Classify this cell by malaria status.
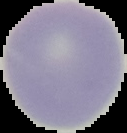

It is uninfected.

Summary:
  - Image type: cell region segmented out of the field of view; surrounding area masked to black
  - Preparation: thin blood smear
  - Image size: 127×133 pixels